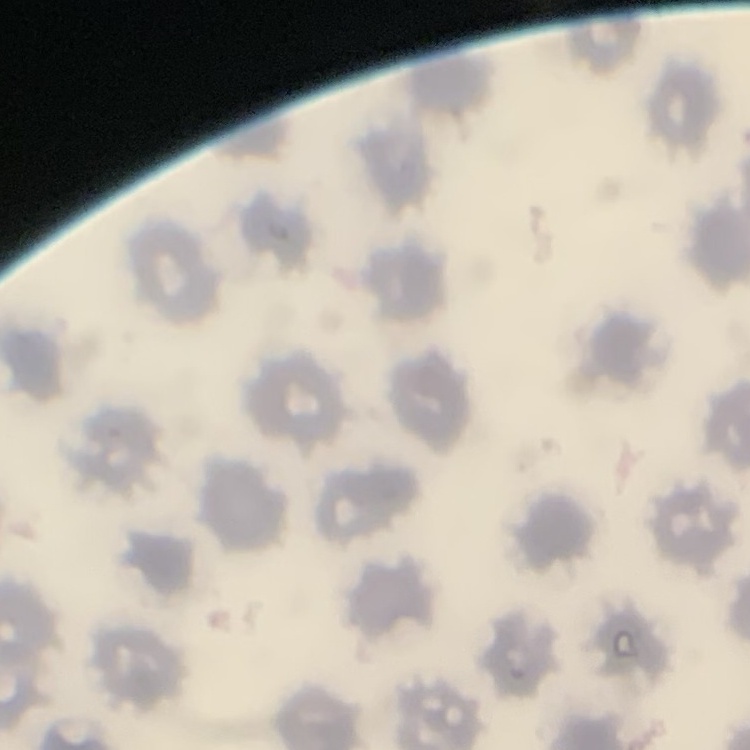
Summary:
  - Red blood cell morphology: no rouleaux formation
  - Preparation: thin blood film
  - Stain: Field's or Giemsa
  - Image type: square crop of a larger photomicrograph